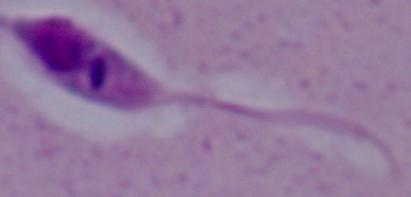
Summary:
  - Identification: Leishmania
  - Magnification: 1000x
  - Modality: micrograph